Give the position of every Plasmodium parasite.
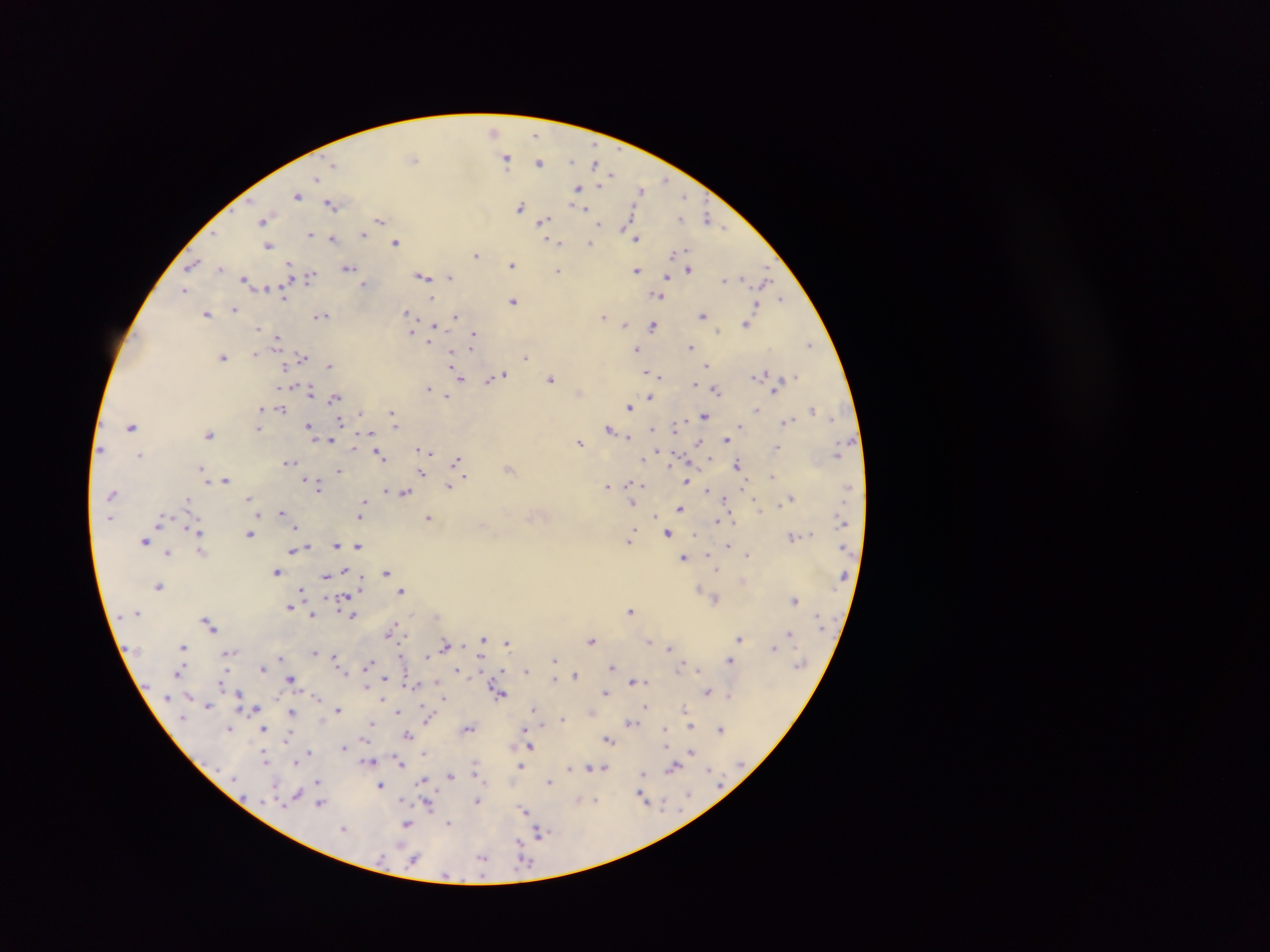
Approximate centers as [x, y] in pixels.
Plasmodium parasites: [493, 130], [535, 134], [414, 158], [506, 158], [570, 161], [540, 162], [595, 162], [334, 165], [611, 175], [317, 178], [666, 180], [577, 188], [640, 190], [297, 195], [684, 196], [331, 204], [521, 206], [584, 209], [707, 217], [681, 219], [263, 220], [380, 220], [542, 221], [626, 223], [600, 224], [723, 227], [629, 230], [311, 233], [364, 234], [333, 238], [637, 238], [396, 242], [555, 242], [589, 243], [268, 245], [476, 254], [192, 264], [289, 265], [512, 265], [219, 268], [347, 268], [689, 269], [557, 270], [636, 271], [311, 276], [422, 276], [667, 276], [450, 277], [245, 279], [725, 279], [764, 280], [364, 283], [267, 288], [184, 290], [284, 294], [657, 295], [782, 298], [431, 299], [513, 301], [235, 309], [407, 313], [207, 314], [322, 316], [455, 316], [603, 316], [703, 316], [746, 323], [625, 325], [653, 326], [258, 328], [434, 328], [411, 332], [277, 338], [474, 339], [809, 344], [471, 345], [691, 347], [636, 349], [255, 353], [223, 357], [302, 357], [451, 357], [525, 357], [329, 365], [706, 365], [284, 366], [649, 372], [761, 374], [660, 376], [795, 376], [497, 377], [459, 378], [552, 379], [489, 380], [695, 384], [427, 387], [715, 390], [310, 391], [447, 395], [334, 397], [649, 398], [629, 407], [261, 408], [281, 409], [757, 409], [812, 409], [392, 413], [704, 415], [394, 420], [787, 421], [340, 422], [395, 425], [132, 426], [741, 426], [310, 427], [675, 427], [259, 428], [609, 429], [209, 434], [628, 438], [726, 439], [329, 440], [699, 441], [580, 442], [354, 445], [777, 447], [420, 450], [427, 451], [380, 454], [140, 455], [643, 459], [457, 461], [289, 462], [737, 464], [201, 469], [508, 469], [339, 470], [204, 472], [421, 473], [772, 476], [226, 479], [305, 481], [685, 481], [630, 484], [450, 486], [608, 486], [318, 487], [707, 490], [404, 492], [111, 494], [249, 498], [725, 498], [791, 498], [187, 499], [363, 503], [633, 504], [680, 509], [760, 509], [282, 512], [361, 513], [257, 514], [655, 517], [429, 518], [730, 518], [160, 520], [717, 521], [295, 527], [196, 532], [668, 533], [250, 534], [632, 535], [791, 536], [630, 540], [144, 541], [336, 544], [358, 546], [729, 546], [294, 550], [201, 551], [168, 553], [708, 555], [747, 555], [683, 558], [716, 570], [346, 571], [277, 572], [386, 572], [326, 576], [158, 585], [301, 591], [402, 591], [345, 599], [716, 599], [794, 600], [289, 607], [631, 610], [312, 616], [352, 616], [209, 625], [392, 627], [790, 633], [740, 638], [483, 639], [592, 641], [649, 642], [507, 643], [446, 644], [183, 646], [669, 648], [774, 648], [314, 652], [228, 654], [335, 656], [427, 656], [281, 658], [555, 659], [730, 660], [369, 663], [612, 666], [262, 668], [680, 668], [698, 669], [179, 671], [458, 671], [525, 671], [575, 674], [385, 678], [291, 679], [554, 679], [635, 681], [436, 682], [366, 686], [707, 691], [605, 692], [499, 694], [239, 695], [729, 695], [442, 696], [445, 699], [208, 705], [645, 707], [684, 708], [254, 709], [534, 709], [338, 710], [398, 711], [291, 713], [429, 715], [563, 718], [631, 722], [370, 723], [542, 725], [690, 727], [229, 729], [263, 729], [469, 729], [665, 729], [721, 729], [408, 734], [288, 737], [609, 740], [530, 746], [344, 747], [310, 752], [424, 752], [691, 752], [264, 757], [369, 761], [296, 762], [400, 763], [522, 766], [475, 767], [592, 767], [570, 768], [603, 768], [673, 768], [709, 769], [643, 773], [451, 776], [318, 782], [549, 782], [423, 783], [380, 785], [642, 795], [688, 795], [296, 796], [403, 799], [578, 800], [594, 800], [477, 801], [321, 803], [428, 804], [524, 811], [449, 823], [406, 824], [343, 829], [541, 832], [519, 842], [482, 858], [414, 860].

Summary:
  - Field of view: single
  - Country: Ghana
  - Capture: mobile-phone photograph through a microscope
  - Preparation: thick blood smear
  - Image size: 1270×952 pixels